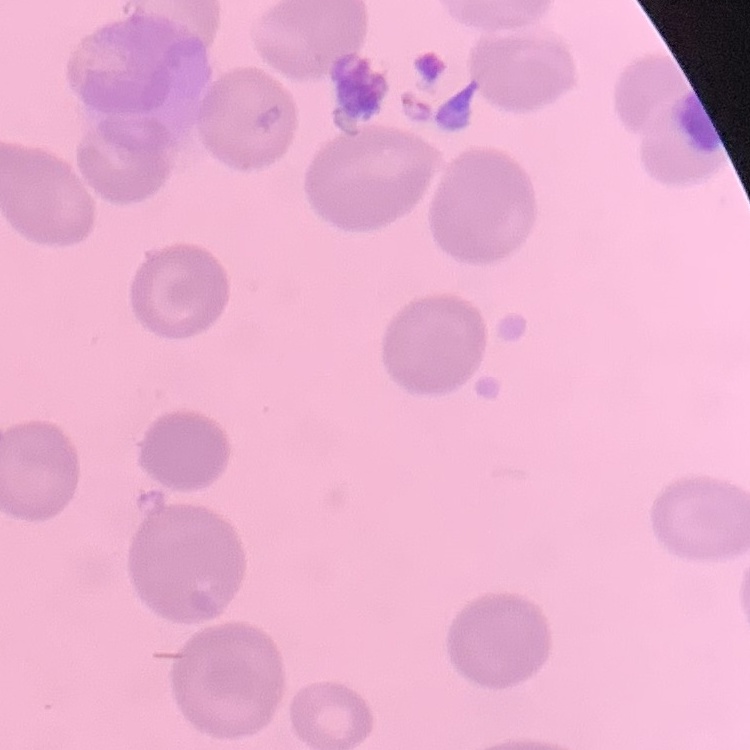
Summary:
  - Erythrocyte morphology: no rouleaux formation
  - Stain: Field's or Giemsa
  - Image type: square crop of a larger photomicrograph
  - Preparation: thin peripheral smear